Point out leukocytes.
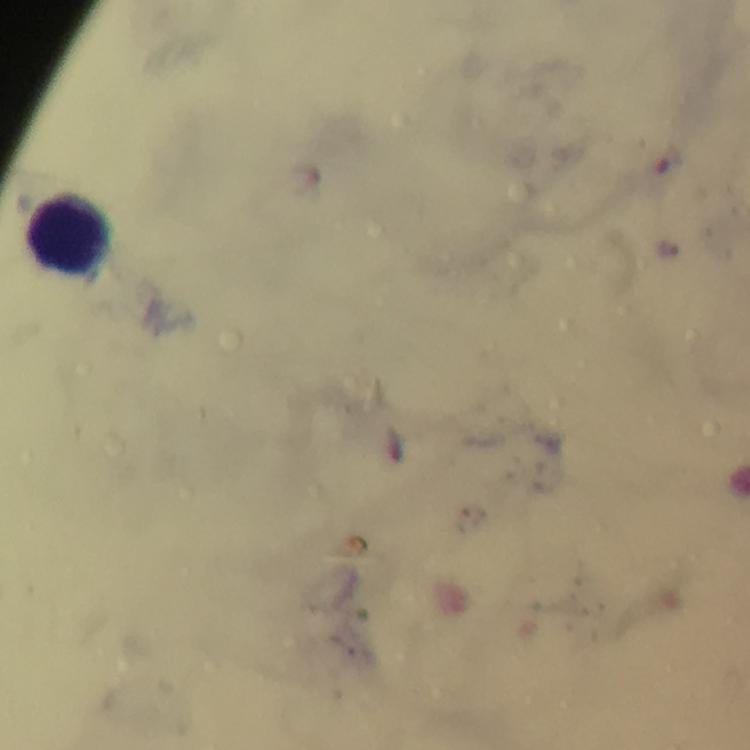
Approximate centers as [x, y] in pixels.
Leukocytes: [67, 232].

Summary:
  - Stain: Giemsa
  - Immersion oil: used
  - Context: from a diagnostic examination for malaria
  - Plasmodium parasites: none seen
  - Magnification: 100x
  - Preparation: thick blood film
  - Capture: smartphone photograph through a microscope
  - Image size: 750×750 pixels
  - Cropped from: one field of view